Describe the morphology of the erythrocytes.
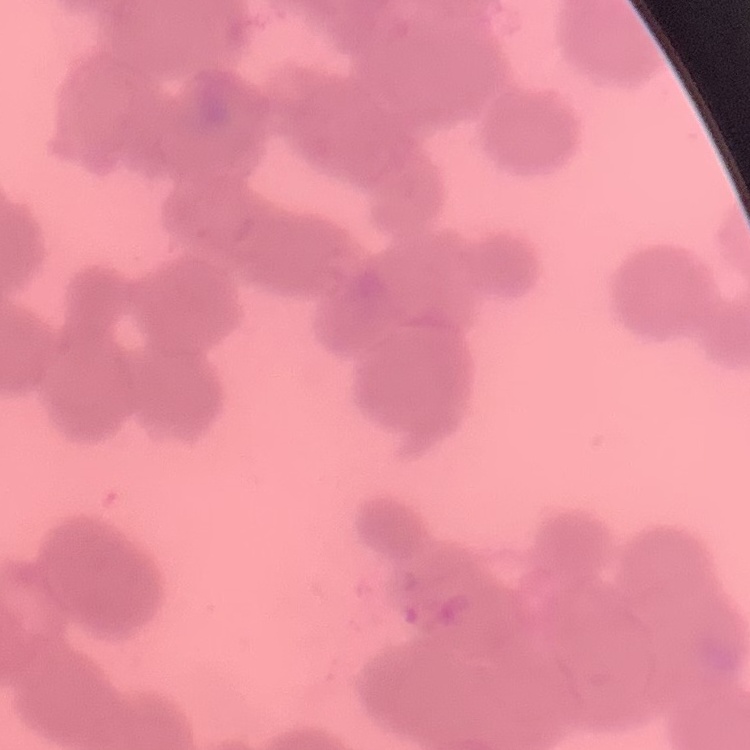

Rouleaux formation.

Thin peripheral smear. Stained with either Field's or Giemsa. One tile cut from a larger photomicrograph.